Assess this cell for malaria.
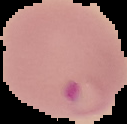
Parasitized.

Image is 127×124 pixels. The area outside the segmented cell region is set to black. From a thin blood smear.